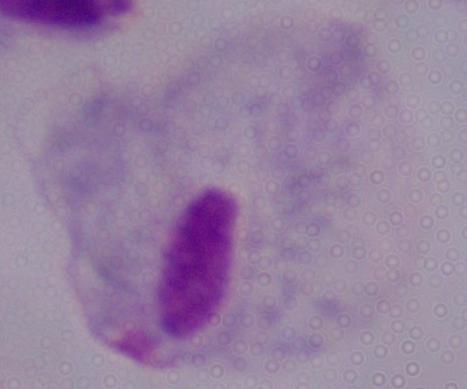

Micrograph. A trichomonad is seen. 1000x magnification.